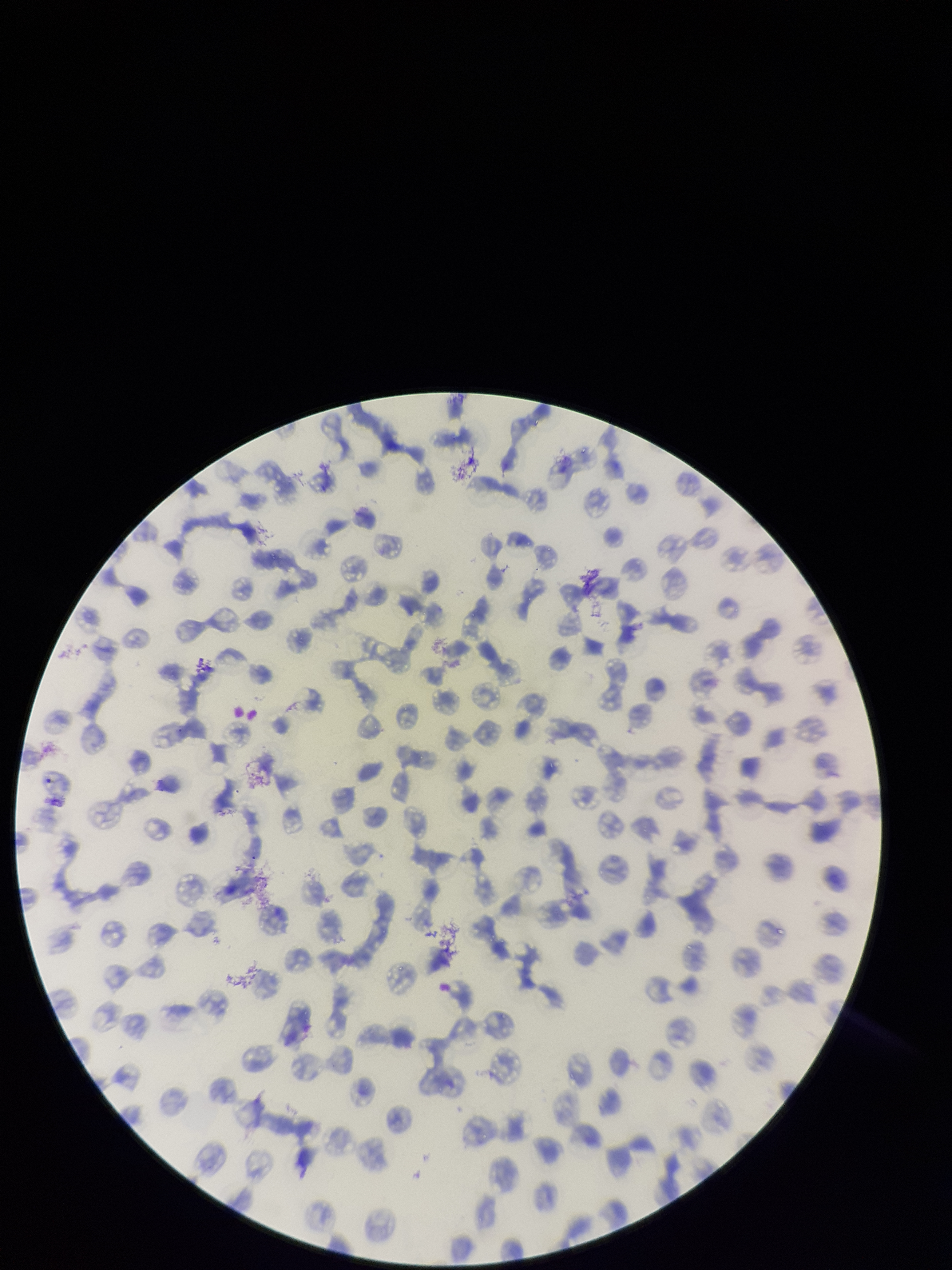

Parasitized red blood cells: none seen. One field from this slide. Parasitized red blood cell count: 0. Patient malaria status: infected. Smartphone photograph taken through the eyepiece of a microscope. Red blood cell count: 167. Image is 952×1270 pixels. Preparation: thin smear. Giemsa stain. Species reported for this patient: Plasmodium falciparum.